Classify this cell by malaria status.
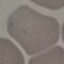

It is uninfected.

Photographed with a smartphone camera at the microscope eyepiece. Automatically extracted cell patch, resized to 64 × 64 pixels. Giemsa-stained preparation. Thin smear of blood.